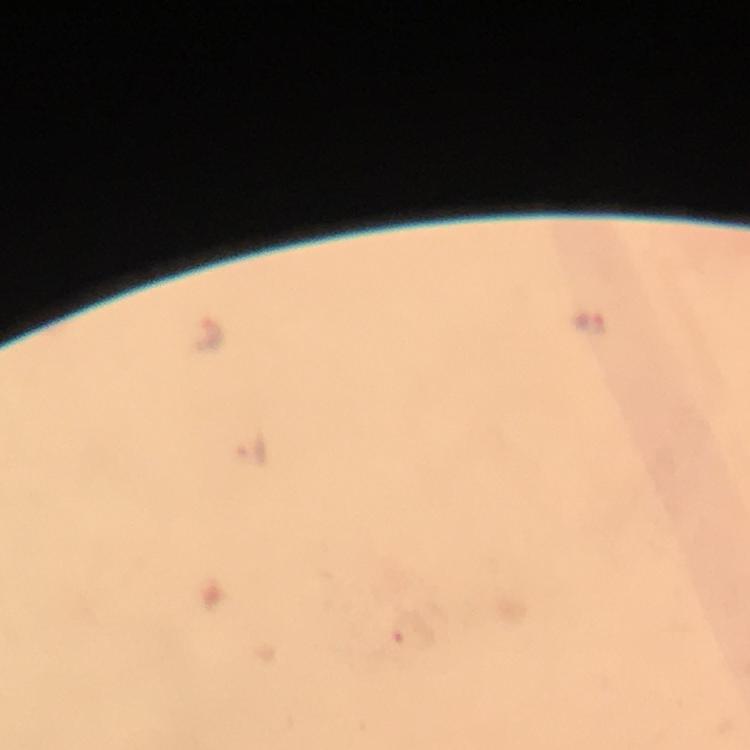 Approximate centers as [x, y] in pixels. Plasmodium parasite locations: [207, 336], [410, 632]. Image is 750×750 pixels. A crop from one field of view. From a diagnostic examination for malaria. At 100x magnification. Smartphone photograph taken through a microscope. Giemsa-stained preparation. Thick blood film. Immersion oil applied.